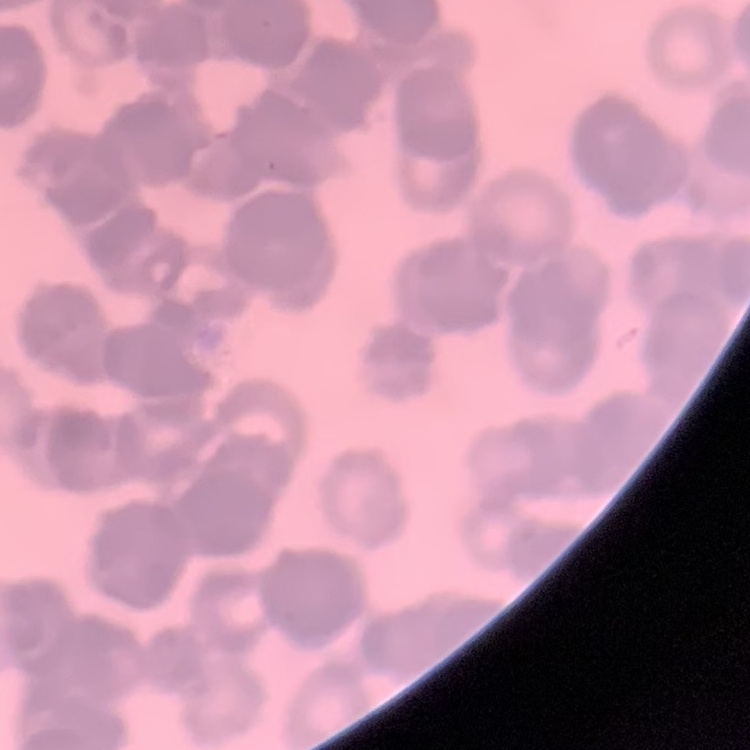
red blood cell morphology = rouleaux formation
preparation = thin blood smear
stain = Field's or Giemsa
image type = square crop of a larger photomicrograph